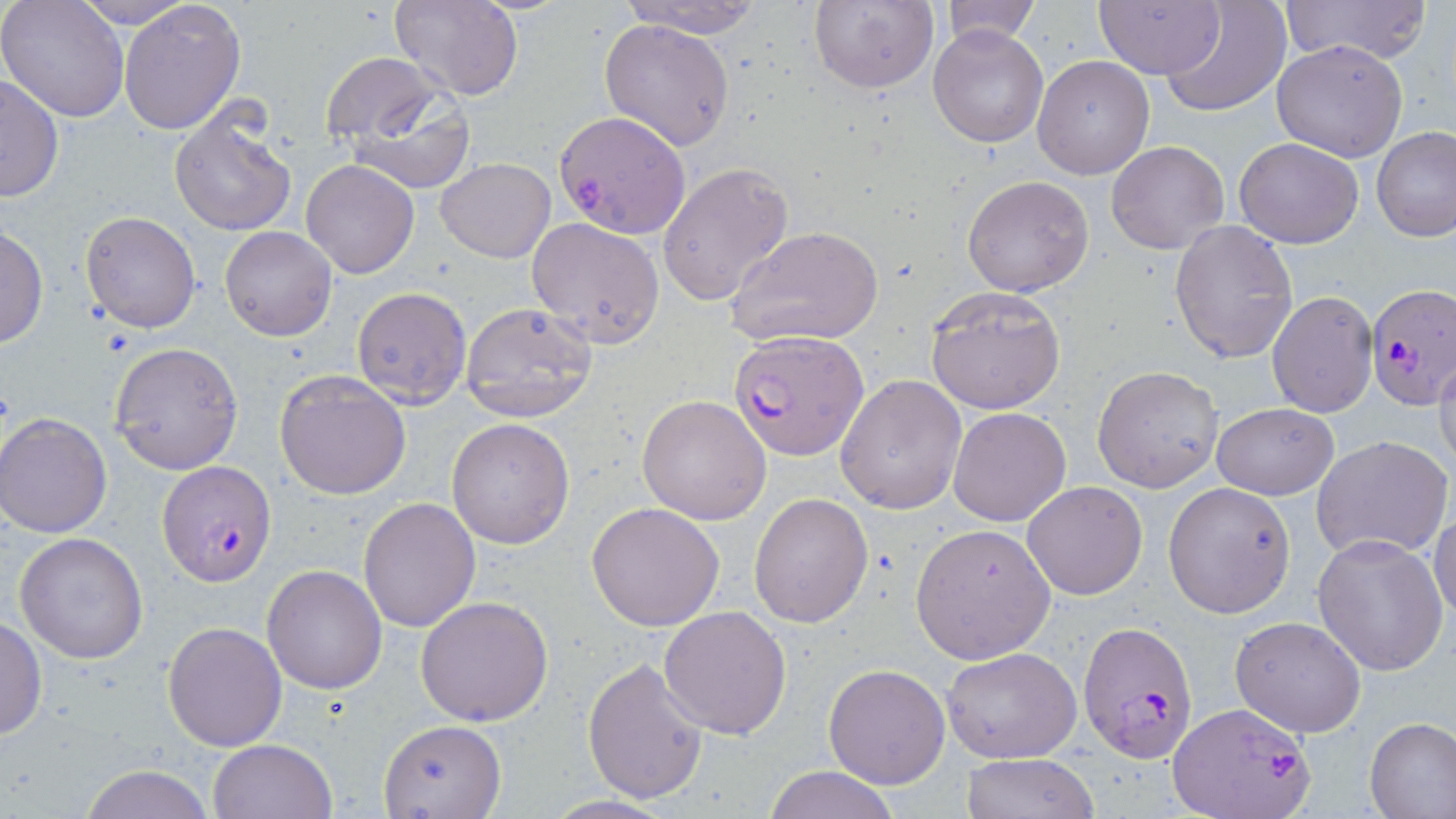

Summary:
  - Coordinate format: approximate bounding boxes as (x1, y1, x2, y2) in pixels
  - Uninfected red blood cell locations: (0, 0, 129, 120), (68, 0, 200, 28), (119, 0, 246, 135), (390, 0, 523, 100), (614, 0, 768, 37), (809, 0, 938, 91), (1095, 0, 1224, 79), (1160, 0, 1290, 117), (1288, 0, 1430, 66), (935, 1, 1042, 47), (599, 18, 734, 151), (929, 23, 1049, 148), (1272, 40, 1408, 162), (320, 54, 444, 144), (1032, 56, 1154, 179), (1, 73, 65, 203), (342, 82, 477, 194), (168, 106, 295, 237), (1372, 127, 1456, 243), (1234, 138, 1363, 248), (1106, 140, 1229, 255), (435, 157, 555, 263), (300, 159, 420, 279), (656, 163, 794, 307), (962, 174, 1095, 296), (80, 211, 201, 332), (526, 218, 666, 347), (1169, 219, 1298, 364), (0, 224, 47, 349), (219, 225, 337, 342), (727, 225, 884, 348), (351, 285, 471, 410), (924, 287, 1067, 413), (1266, 291, 1377, 416), (460, 302, 597, 422), (108, 342, 243, 473), (1433, 349, 1456, 474), (1092, 365, 1223, 493), (275, 370, 410, 499), (834, 373, 967, 516), (639, 393, 772, 524), (1212, 402, 1339, 499), (949, 407, 1072, 527), (1, 415, 112, 539), (447, 418, 575, 549), (1313, 435, 1453, 561), (1022, 481, 1149, 601), (1163, 481, 1295, 619), (749, 493, 874, 628), (358, 496, 483, 632), (586, 502, 727, 631), (1430, 506, 1456, 625), (910, 523, 1055, 662), (14, 531, 149, 664), (1312, 534, 1448, 676), (261, 565, 387, 694), (414, 595, 554, 725), (658, 606, 792, 738), (1, 614, 45, 743), (1231, 616, 1366, 738), (162, 622, 286, 751), (938, 647, 1083, 765), (581, 657, 709, 804), (823, 663, 950, 790), (1365, 717, 1456, 817), (378, 719, 507, 817), (208, 739, 337, 819), (960, 754, 1102, 818), (79, 765, 216, 819), (761, 766, 899, 819), (542, 794, 678, 818)
  - Plasmodium falciparum-infected red blood cell locations: (554, 110, 691, 239), (1366, 285, 1455, 409), (729, 327, 868, 462), (158, 459, 277, 585), (1077, 620, 1198, 764), (1170, 700, 1313, 819)
  - Slide-level diagnosis: Plasmodium falciparum
  - Image size: 1456×819 pixels
  - Magnification: 1000x
  - Preparation: thin blood film
  - Field of view: single
  - Stain: May-Grünwald-Giemsa
  - Modality: light microscopy